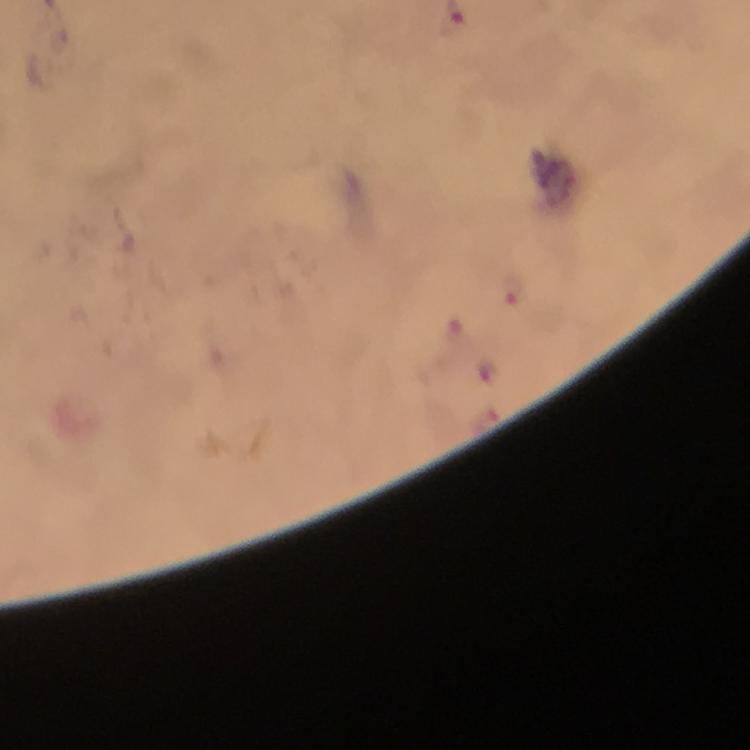
Approximate centers as [x, y] in pixels.
Summary:
  - Malaria parasite locations: [515, 289]
  - Image size: 750×750 pixels
  - Capture: smartphone camera through the microscope
  - Cropped from: a single field of view
  - Context: from a malaria diagnostic workup
  - Immersion oil: applied
  - Preparation: thick smear
  - Stain: Giemsa
  - Magnification: 100x